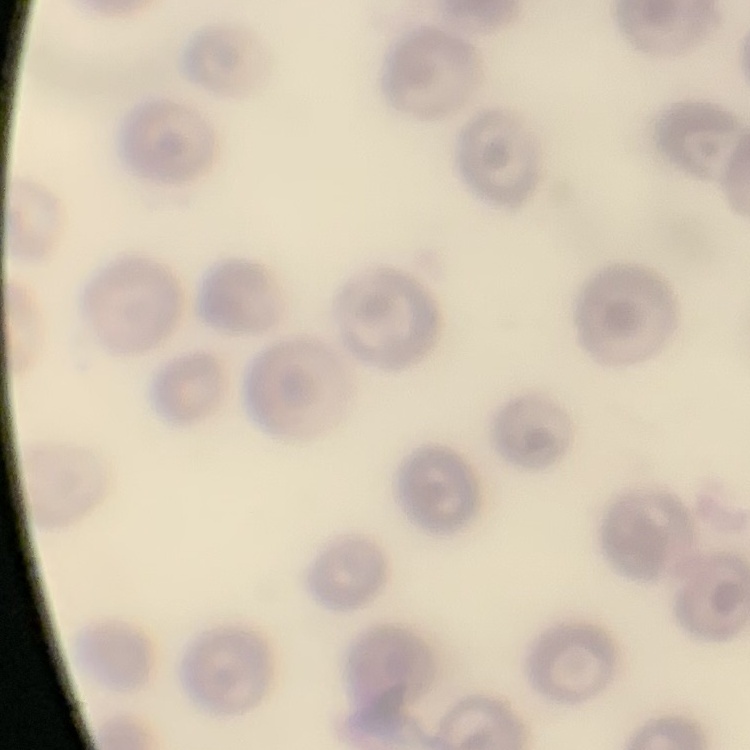

erythrocyte morphology = no rouleaux formation
preparation = thin blood smear
stain = Field's or Giemsa
image type = one tile cut from a larger photomicrograph